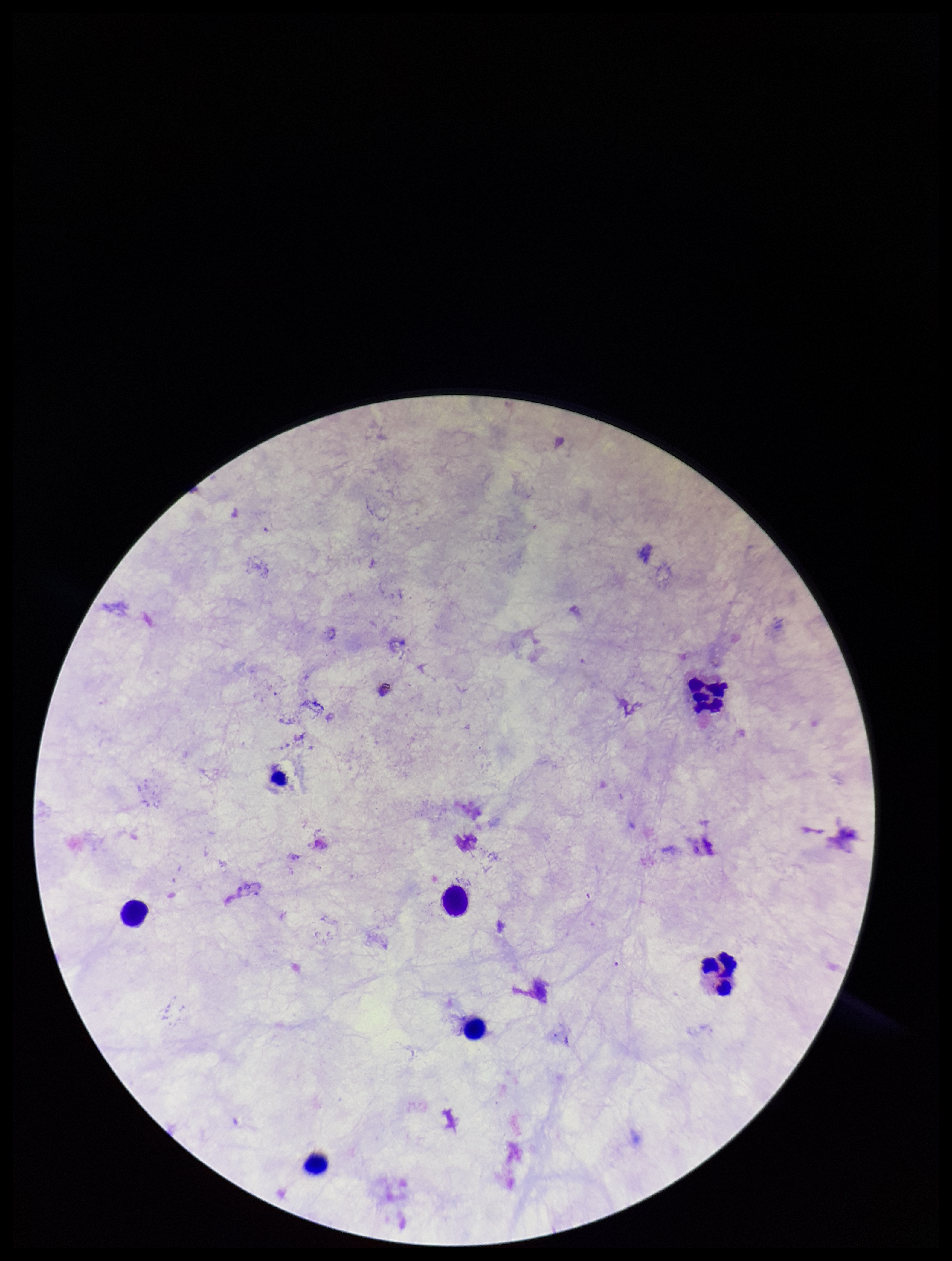 Giemsa stain. Photographed through the microscope eyepiece with a smartphone camera. Parasite count: 0. Single field of view. Preparation: thick smear. Leukocyte count: 6. Image is 952×1261 pixels. Plasmodium parasites: none detected. Patient malaria status: negative.